Outline each blood parasite and name the species.
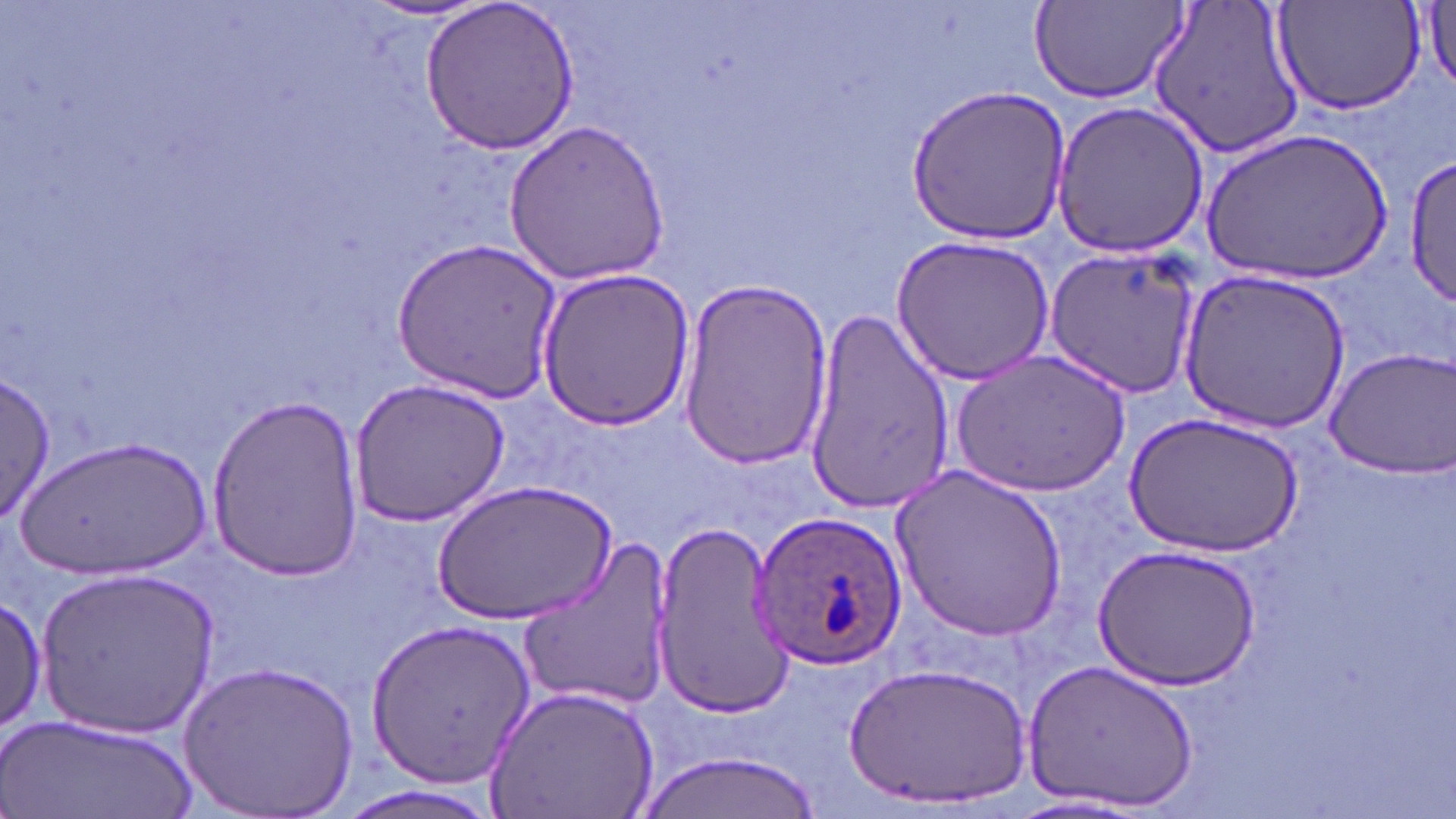
Approximate bounding boxes as named x1/y1/x2/y2 corners in pixels.
Plasmodium ovale-infected red blood cells: (x1=751, y1=511, x2=907, y2=668).
No Plasmodium falciparum, Plasmodium malariae, Plasmodium vivax, Babesia divergens, or Trypanosoma brucei observed.

Uninfected red blood cell locations: (x1=416, y1=0, x2=584, y2=158), (x1=1146, y1=0, x2=1309, y2=160), (x1=1272, y1=0, x2=1428, y2=118), (x1=1415, y1=0, x2=1456, y2=97), (x1=358, y1=2, x2=494, y2=24), (x1=1028, y1=2, x2=1187, y2=104), (x1=906, y1=84, x2=1070, y2=245), (x1=1052, y1=100, x2=1210, y2=260), (x1=501, y1=119, x2=671, y2=284), (x1=1203, y1=131, x2=1392, y2=282), (x1=1406, y1=157, x2=1455, y2=308), (x1=891, y1=236, x2=1055, y2=386), (x1=389, y1=237, x2=563, y2=401), (x1=1045, y1=247, x2=1201, y2=399), (x1=535, y1=266, x2=695, y2=432), (x1=1177, y1=268, x2=1350, y2=435), (x1=677, y1=279, x2=835, y2=468), (x1=802, y1=301, x2=955, y2=517), (x1=1322, y1=345, x2=1456, y2=478), (x1=952, y1=350, x2=1130, y2=495), (x1=0, y1=368, x2=56, y2=530), (x1=349, y1=378, x2=512, y2=529), (x1=207, y1=394, x2=365, y2=581), (x1=1126, y1=410, x2=1304, y2=558), (x1=21, y1=436, x2=211, y2=578), (x1=887, y1=465, x2=1065, y2=640), (x1=433, y1=479, x2=616, y2=623), (x1=652, y1=519, x2=800, y2=713), (x1=516, y1=539, x2=675, y2=714), (x1=1094, y1=545, x2=1260, y2=689), (x1=38, y1=568, x2=220, y2=737), (x1=0, y1=593, x2=47, y2=740), (x1=363, y1=617, x2=537, y2=794), (x1=1024, y1=657, x2=1199, y2=814), (x1=181, y1=658, x2=360, y2=816), (x1=847, y1=662, x2=1033, y2=810), (x1=484, y1=683, x2=660, y2=819), (x1=6, y1=713, x2=199, y2=818), (x1=635, y1=750, x2=826, y2=819), (x1=1004, y1=794, x2=1161, y2=818). Slide-level diagnosis: Plasmodium ovale. Light microscopy. 1000x magnification. Thin blood smear. May-Grünwald-Giemsa stain. Single field of view. Image is 1456×819 pixels.